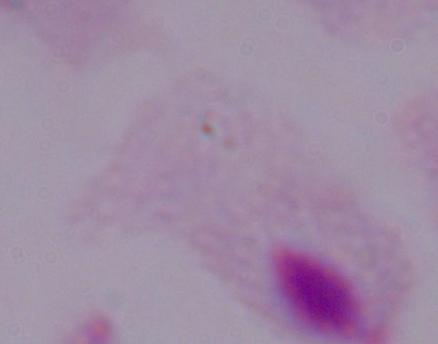
A trichomonad is shown. Micrograph. Captured at 1000x magnification.